Identify the preparation type.
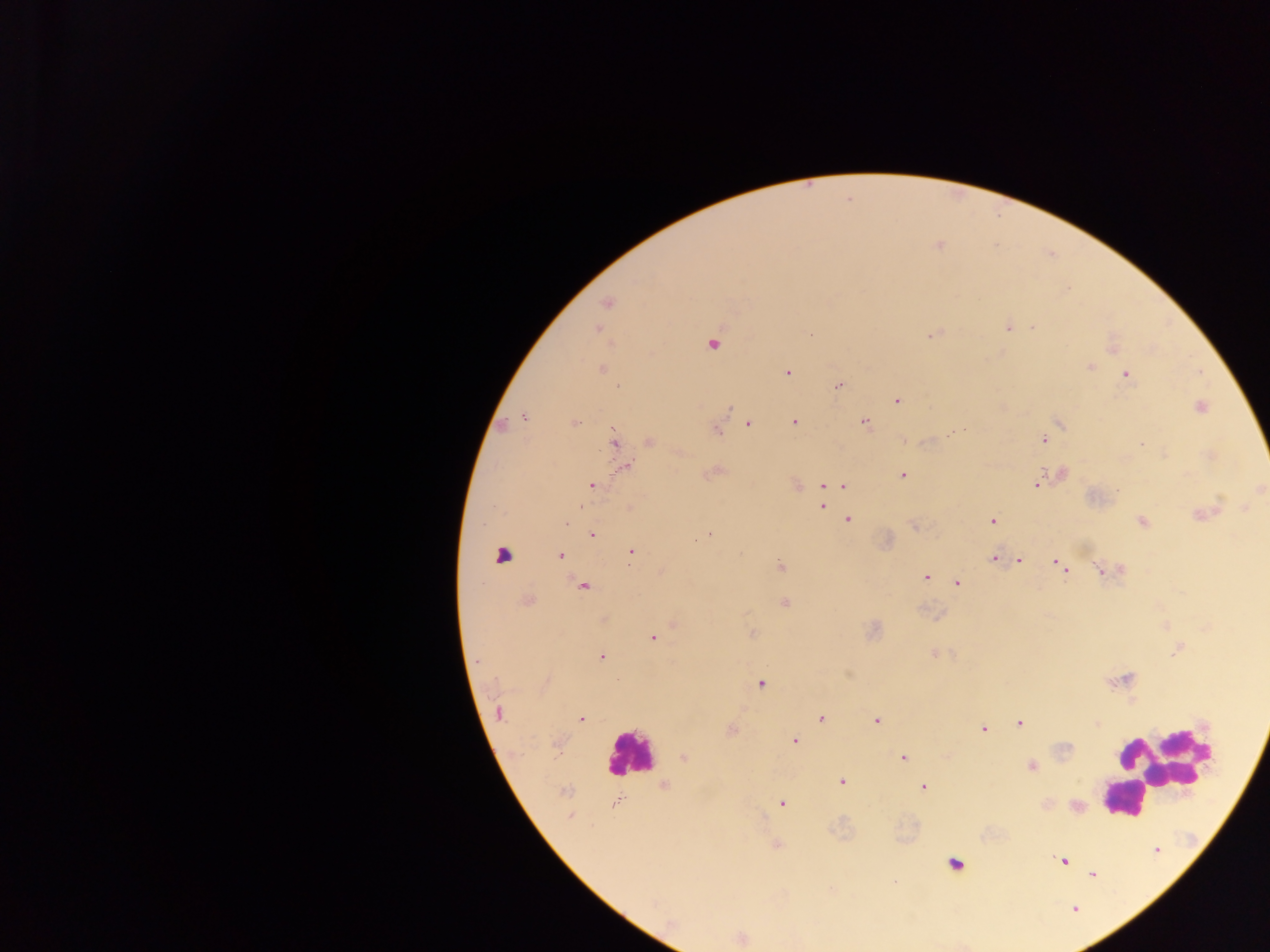
Thick blood film.

Approximate centers as [x, y] in pixels. Leukocyte locations: [629, 753], [1161, 765], [1125, 798], [955, 864]. Plasmodium parasite locations: [938, 245], [607, 302], [1008, 327], [1031, 327], [597, 329], [932, 335], [712, 343], [1111, 344], [1089, 367], [601, 369], [788, 372], [1125, 374], [838, 385], [897, 399], [1200, 407], [730, 408], [523, 416], [1059, 421], [794, 422], [573, 423], [864, 423], [748, 424], [963, 429], [716, 430], [1042, 438], [614, 440], [905, 440], [649, 441], [1211, 455], [625, 466], [712, 471], [902, 474], [1061, 474], [1037, 483], [795, 484], [592, 485], [822, 485], [843, 485], [1259, 488], [821, 495], [821, 505], [1244, 508], [1203, 515], [847, 519], [993, 521], [1141, 521], [566, 522], [915, 526], [591, 534], [708, 534], [631, 551], [559, 555], [995, 558], [1019, 560], [1057, 561], [1060, 565], [781, 566], [1121, 568], [661, 571], [1100, 571], [925, 576], [957, 582], [582, 585], [525, 600], [784, 603], [604, 619], [674, 623], [873, 629], [751, 633], [653, 637], [1178, 648], [933, 653], [601, 657], [1120, 680], [761, 684], [498, 713], [821, 717], [581, 719], [876, 719], [1019, 723], [1096, 723], [982, 729], [731, 730], [794, 740], [557, 743], [683, 757], [902, 757], [1032, 766], [842, 781], [664, 785], [924, 787], [564, 791], [615, 802], [781, 803], [1076, 807], [570, 815], [776, 845], [1155, 850], [1064, 860], [1092, 874], [893, 882], [1074, 908], [740, 938]. Object labeled both Plasmodium parasite and leukocyte by the source: [502, 555]. Sample from Ghana. Mobile-phone photograph taken through the microscope. Image is 1270×952 pixels. One field of view.